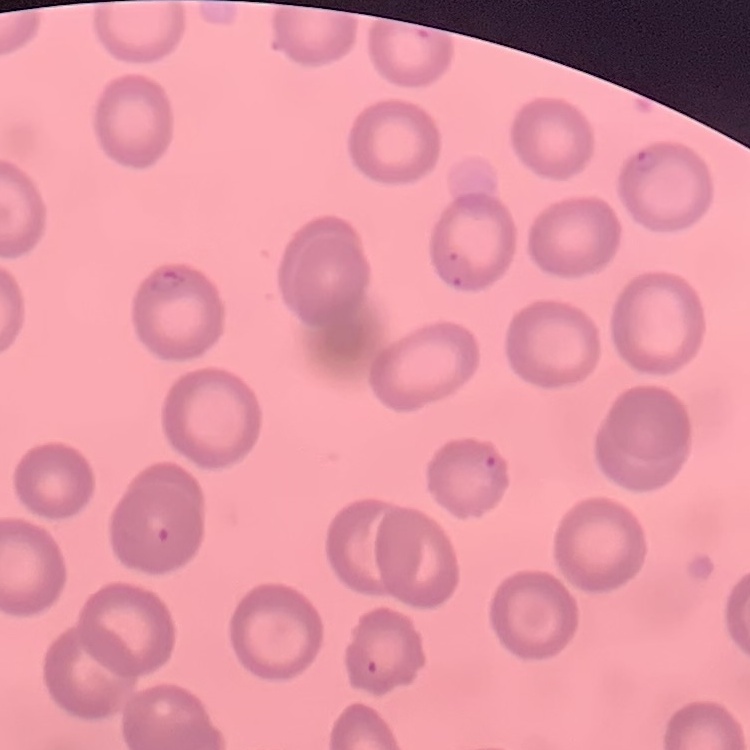 The erythrocytes show no rouleaux formation. Square crop of a larger photomicrograph. Thin blood smear. Field's or Giemsa stain.